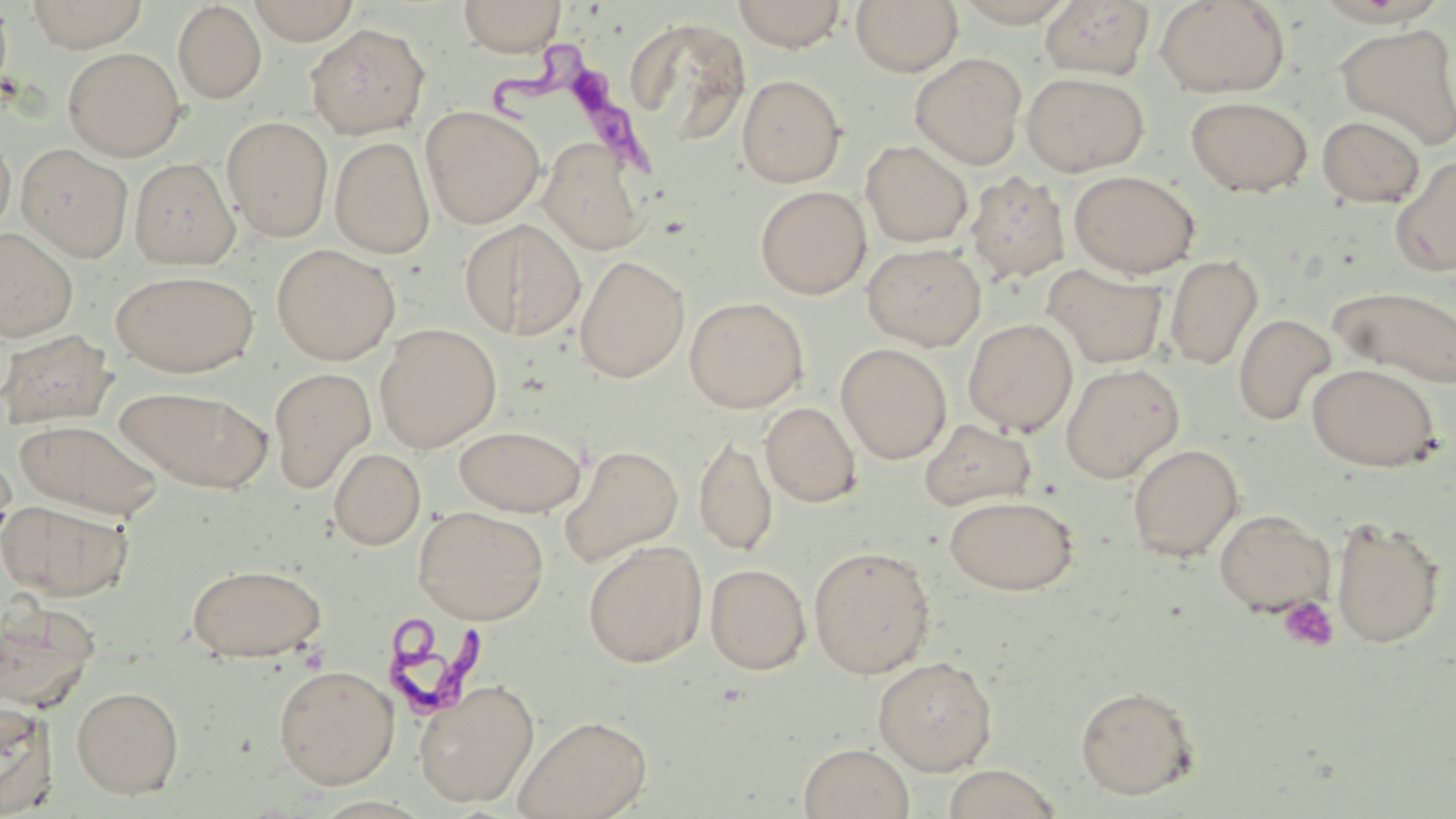

Summary:
  - Coordinate format: approximate bounding boxes as named x1/y1/x2/y2 corners in pixels
  - Uninfected red blood cell locations: (x1=25, y1=0, x2=149, y2=52), (x1=248, y1=0, x2=359, y2=44), (x1=458, y1=0, x2=566, y2=57), (x1=731, y1=0, x2=848, y2=51), (x1=851, y1=0, x2=963, y2=76), (x1=953, y1=0, x2=1079, y2=27), (x1=1155, y1=0, x2=1289, y2=97), (x1=0, y1=1, x2=13, y2=99), (x1=1039, y1=1, x2=1155, y2=80), (x1=172, y1=2, x2=266, y2=103), (x1=620, y1=15, x2=754, y2=158), (x1=306, y1=23, x2=429, y2=139), (x1=1334, y1=23, x2=1456, y2=151), (x1=63, y1=48, x2=185, y2=161), (x1=910, y1=53, x2=1027, y2=170), (x1=1022, y1=72, x2=1149, y2=177), (x1=737, y1=75, x2=846, y2=187), (x1=1185, y1=96, x2=1312, y2=197), (x1=421, y1=105, x2=544, y2=229), (x1=1317, y1=115, x2=1425, y2=207), (x1=222, y1=116, x2=333, y2=241), (x1=0, y1=130, x2=15, y2=236), (x1=331, y1=136, x2=435, y2=258), (x1=539, y1=139, x2=647, y2=255), (x1=861, y1=141, x2=973, y2=247), (x1=16, y1=143, x2=134, y2=262), (x1=1391, y1=155, x2=1456, y2=277), (x1=130, y1=158, x2=238, y2=268), (x1=1069, y1=170, x2=1199, y2=277), (x1=966, y1=172, x2=1071, y2=283), (x1=755, y1=186, x2=871, y2=299), (x1=460, y1=219, x2=586, y2=339), (x1=0, y1=229, x2=78, y2=342), (x1=862, y1=243, x2=986, y2=351), (x1=271, y1=244, x2=400, y2=365), (x1=1165, y1=254, x2=1263, y2=371), (x1=574, y1=255, x2=689, y2=383), (x1=1044, y1=265, x2=1167, y2=369), (x1=111, y1=270, x2=260, y2=377), (x1=1329, y1=285, x2=1456, y2=389), (x1=684, y1=297, x2=808, y2=413), (x1=1233, y1=313, x2=1336, y2=426), (x1=963, y1=318, x2=1078, y2=435), (x1=375, y1=323, x2=501, y2=452), (x1=1, y1=329, x2=115, y2=429), (x1=835, y1=343, x2=952, y2=464), (x1=1060, y1=363, x2=1184, y2=483), (x1=1307, y1=363, x2=1441, y2=471), (x1=268, y1=367, x2=376, y2=493), (x1=115, y1=386, x2=273, y2=492), (x1=761, y1=402, x2=861, y2=507), (x1=15, y1=418, x2=164, y2=519), (x1=920, y1=419, x2=1035, y2=511), (x1=455, y1=425, x2=585, y2=516), (x1=695, y1=434, x2=777, y2=556), (x1=559, y1=444, x2=683, y2=568), (x1=1128, y1=444, x2=1243, y2=561), (x1=329, y1=448, x2=426, y2=549), (x1=0, y1=452, x2=17, y2=558), (x1=945, y1=495, x2=1078, y2=595), (x1=0, y1=499, x2=133, y2=601), (x1=413, y1=506, x2=549, y2=624), (x1=1213, y1=509, x2=1335, y2=615), (x1=1330, y1=517, x2=1446, y2=649), (x1=583, y1=540, x2=707, y2=668), (x1=808, y1=546, x2=935, y2=678), (x1=186, y1=563, x2=326, y2=661), (x1=705, y1=563, x2=811, y2=674), (x1=1, y1=599, x2=100, y2=710), (x1=873, y1=656, x2=998, y2=774), (x1=274, y1=664, x2=399, y2=788), (x1=414, y1=680, x2=539, y2=807), (x1=71, y1=685, x2=184, y2=798), (x1=1075, y1=685, x2=1199, y2=799), (x1=0, y1=700, x2=59, y2=816), (x1=513, y1=714, x2=652, y2=819), (x1=798, y1=743, x2=915, y2=819), (x1=940, y1=765, x2=1063, y2=819)
  - Trypanosoma brucei locations: (x1=489, y1=38, x2=662, y2=179), (x1=387, y1=612, x2=496, y2=715)
  - Platelet locations: (x1=1277, y1=596, x2=1338, y2=653)
  - Slide-level diagnosis: Trypanosoma brucei
  - Magnification: 1000x
  - Field of view: single
  - Preparation: thin blood film
  - Stain: May-Grünwald-Giemsa
  - Modality: optical microscopy
  - Image size: 1456×819 pixels